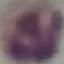
Summary:
  - Malaria status: uninfected
  - Preparation: thin blood smear
  - Image type: automatically extracted cell patch, resized to 64 × 64 pixels
  - Stain: Giemsa
  - Capture: smartphone through the microscope eyepiece